Comment on the morphology of the red blood cells.
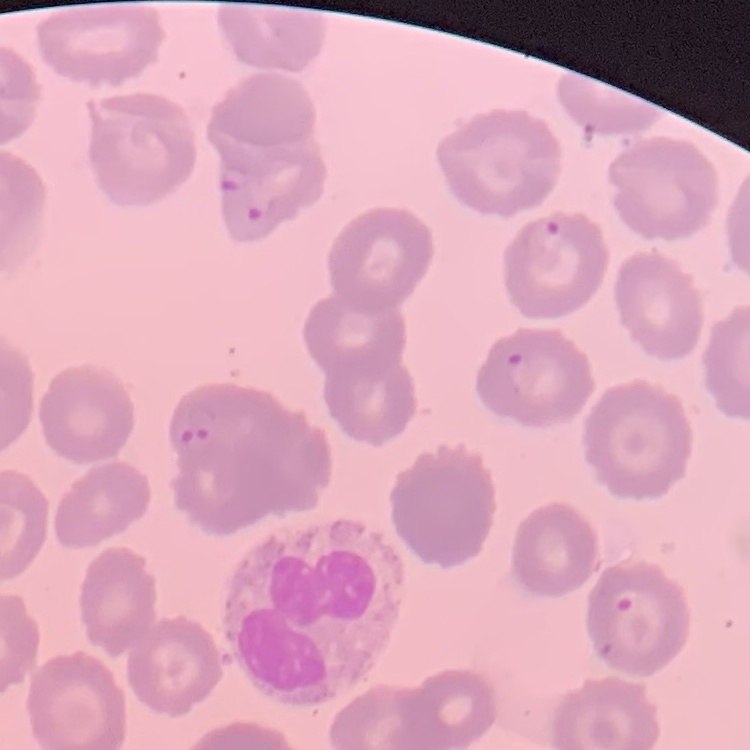

They show no rouleaux formation.

Summary:
  - Preparation: thin peripheral smear
  - Image type: square crop of a larger photomicrograph
  - Stain: Field's or Giemsa